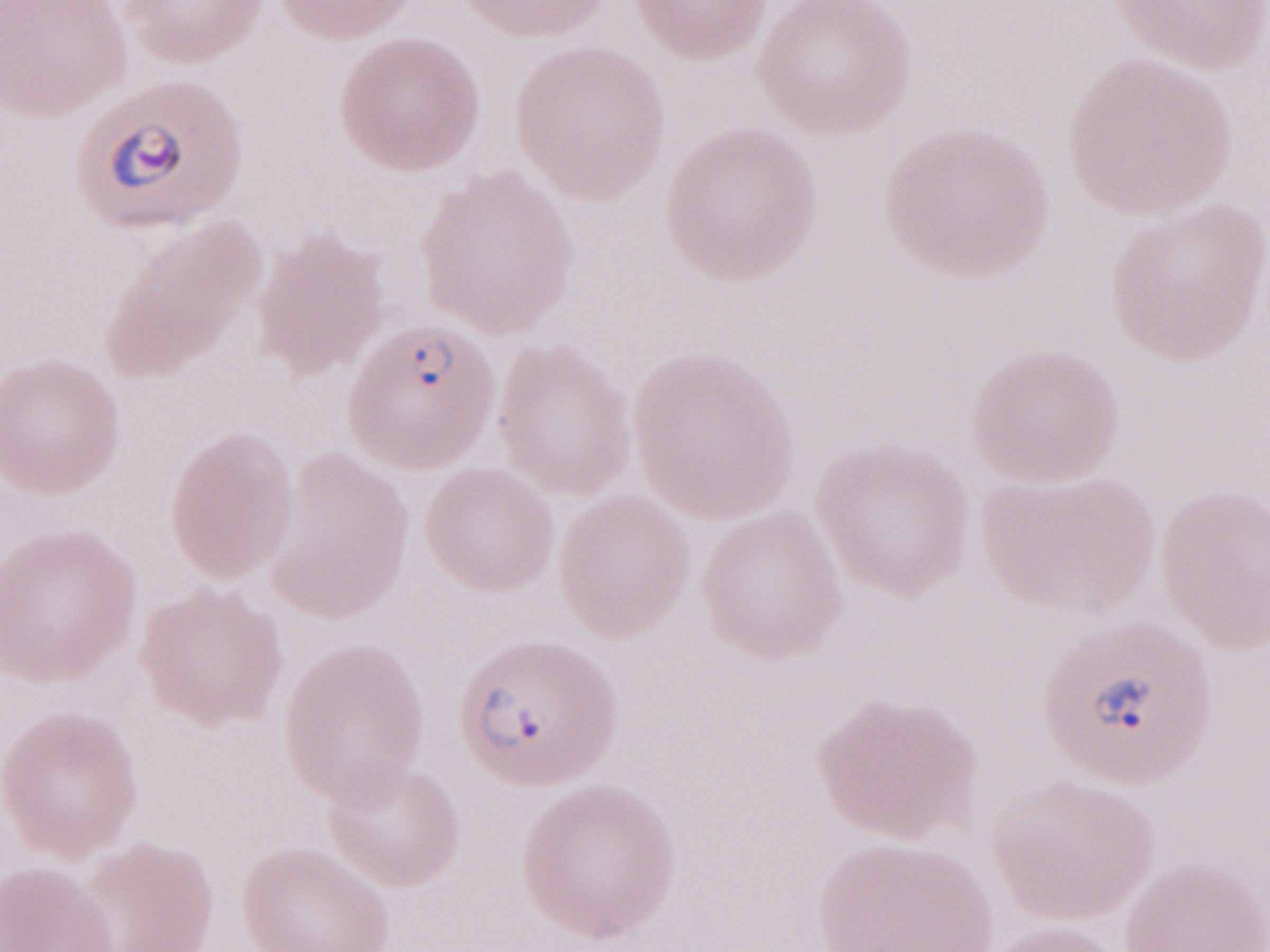

May-Grünwald-Giemsa (MGG) stain. Single field of view. Thin peripheral-blood smear. Olympus BX43 microscope, Olympus DP73 camera. Patient-level malaria diagnosis: positive. Magnification: 1,000x. Image is 1270×952 pixels.